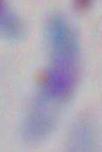
magnification: 1000x
identification: Toxoplasma gondii
modality: micrograph